Locate every uninfected red blood cell.
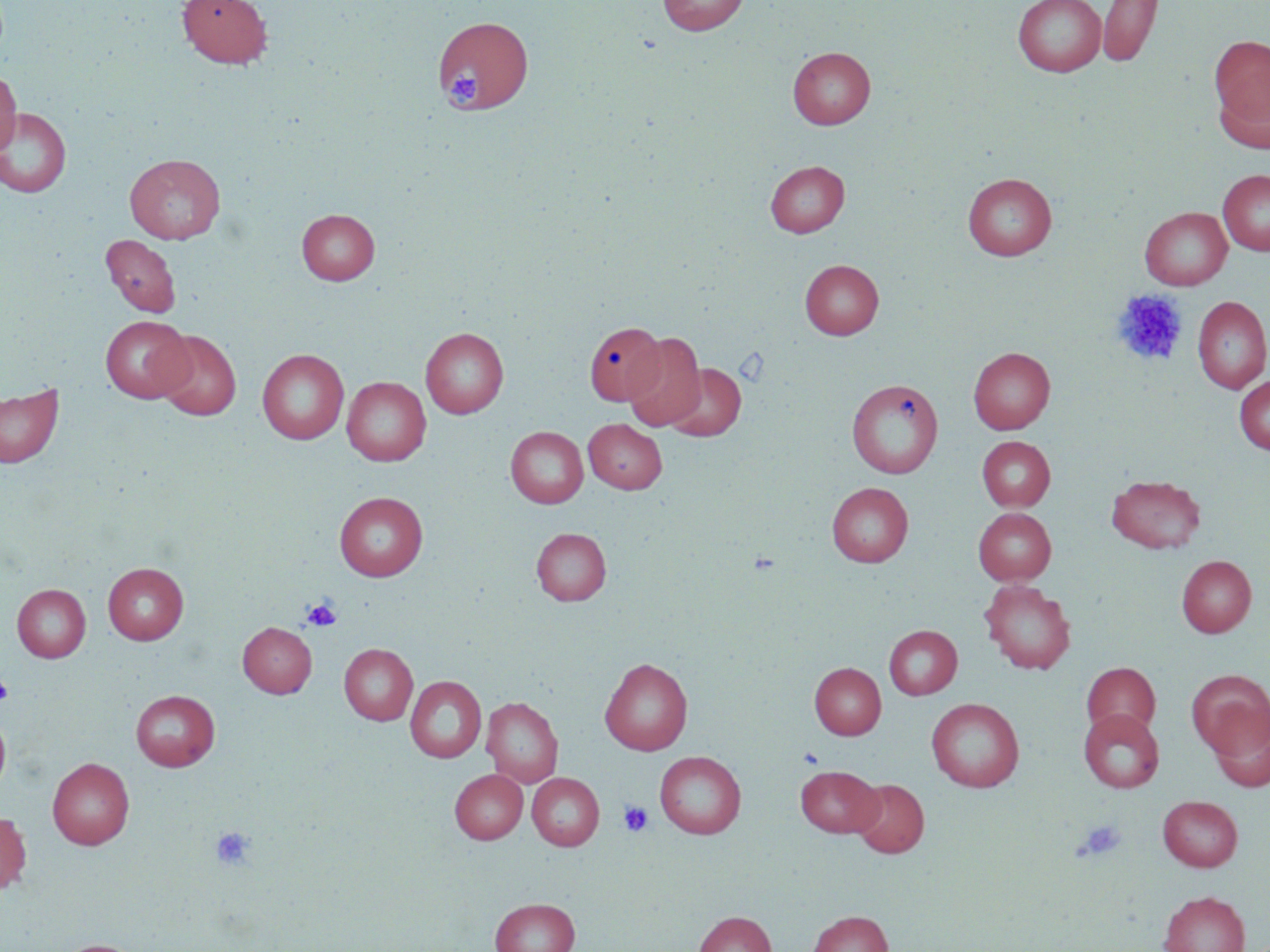

Approximate bounding boxes as named x1/y1/x2/y2 corners in pixels.
Uninfected red blood cells: (x1=176, y1=0, x2=273, y2=69), (x1=657, y1=0, x2=749, y2=35), (x1=1012, y1=0, x2=1106, y2=77), (x1=1097, y1=0, x2=1163, y2=67), (x1=434, y1=15, x2=534, y2=115), (x1=1210, y1=34, x2=1270, y2=133), (x1=788, y1=46, x2=875, y2=129), (x1=0, y1=69, x2=21, y2=158), (x1=1213, y1=76, x2=1270, y2=155), (x1=0, y1=107, x2=72, y2=198), (x1=125, y1=154, x2=225, y2=244), (x1=765, y1=160, x2=849, y2=237), (x1=1218, y1=169, x2=1270, y2=256), (x1=962, y1=172, x2=1057, y2=260), (x1=1140, y1=207, x2=1232, y2=290), (x1=297, y1=208, x2=379, y2=285), (x1=100, y1=234, x2=181, y2=317), (x1=800, y1=259, x2=884, y2=339), (x1=1193, y1=296, x2=1270, y2=393), (x1=100, y1=316, x2=193, y2=403), (x1=584, y1=321, x2=667, y2=406), (x1=421, y1=327, x2=508, y2=418), (x1=153, y1=330, x2=241, y2=421), (x1=623, y1=332, x2=706, y2=431), (x1=968, y1=347, x2=1055, y2=434), (x1=257, y1=349, x2=349, y2=444), (x1=664, y1=363, x2=746, y2=441), (x1=1234, y1=375, x2=1270, y2=455), (x1=342, y1=376, x2=431, y2=466), (x1=847, y1=378, x2=944, y2=478), (x1=0, y1=383, x2=63, y2=468), (x1=584, y1=418, x2=667, y2=494), (x1=505, y1=426, x2=588, y2=508), (x1=977, y1=436, x2=1055, y2=510), (x1=1106, y1=474, x2=1206, y2=553), (x1=827, y1=482, x2=913, y2=566), (x1=334, y1=491, x2=428, y2=580), (x1=973, y1=508, x2=1056, y2=584), (x1=531, y1=527, x2=611, y2=605), (x1=1177, y1=555, x2=1256, y2=637), (x1=103, y1=562, x2=188, y2=644), (x1=980, y1=580, x2=1076, y2=675), (x1=12, y1=584, x2=91, y2=663), (x1=238, y1=622, x2=316, y2=698), (x1=884, y1=625, x2=962, y2=699), (x1=339, y1=644, x2=417, y2=725), (x1=600, y1=657, x2=693, y2=755), (x1=809, y1=662, x2=886, y2=739), (x1=1082, y1=662, x2=1160, y2=737), (x1=1187, y1=670, x2=1270, y2=757), (x1=405, y1=675, x2=486, y2=763), (x1=131, y1=690, x2=220, y2=771), (x1=481, y1=697, x2=563, y2=786), (x1=926, y1=698, x2=1024, y2=792), (x1=1208, y1=705, x2=1270, y2=792), (x1=1078, y1=708, x2=1164, y2=793), (x1=0, y1=712, x2=11, y2=794), (x1=654, y1=751, x2=746, y2=838), (x1=48, y1=757, x2=134, y2=849), (x1=795, y1=765, x2=883, y2=837), (x1=450, y1=769, x2=527, y2=843), (x1=527, y1=773, x2=604, y2=851), (x1=850, y1=779, x2=929, y2=858), (x1=1158, y1=795, x2=1243, y2=871), (x1=0, y1=811, x2=31, y2=894), (x1=1160, y1=890, x2=1249, y2=952), (x1=490, y1=898, x2=580, y2=952), (x1=808, y1=910, x2=893, y2=952), (x1=694, y1=911, x2=776, y2=952), (x1=55, y1=939, x2=144, y2=952).

{
  "slide_level_diagnosis": "no evidence of blood parasites",
  "image_size": "1270×952 pixels",
  "magnification": "1000x",
  "platelet_locations": "approximate bounding boxes as named x1/y1/x2/y2 corners in pixels: (x1=444, y1=64, x2=483, y2=111), (x1=1112, y1=290, x2=1188, y2=367), (x1=302, y1=598, x2=341, y2=631), (x1=0, y1=673, x2=13, y2=704), (x1=799, y1=747, x2=824, y2=767), (x1=618, y1=801, x2=653, y2=837), (x1=1076, y1=819, x2=1127, y2=861), (x1=210, y1=827, x2=255, y2=870)",
  "field_of_view": "one of a larger specimen",
  "modality": "light microscopy",
  "stain": "May-Grünwald-Giemsa",
  "preparation": "thin blood smear"
}